Assess the morphology of the red blood cells.
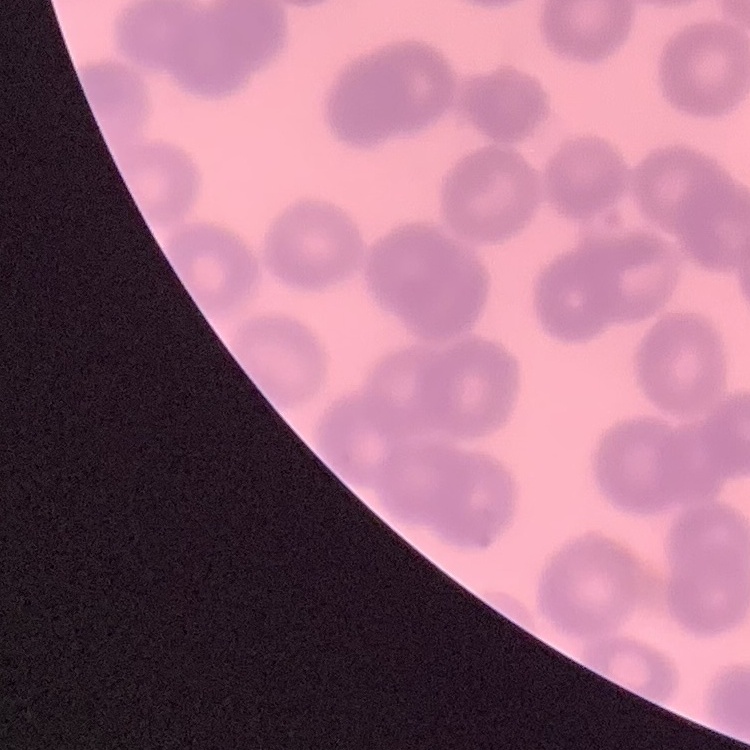

They show no rouleaux formation.

preparation: thin blood smear
image_type: one tile cut from a larger photomicrograph
stain: Field's or Giemsa